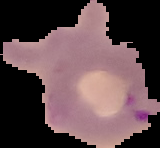
Image is 160×148 pixels. Result: Plasmodium parasites detected. Cell region segmented out of the field of view; the surrounding area is masked to black. From a thin blood smear.